Name the parasite shown.
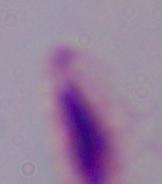
This is a trichomonad.

Captured at 1000x magnification. Photomicrograph.